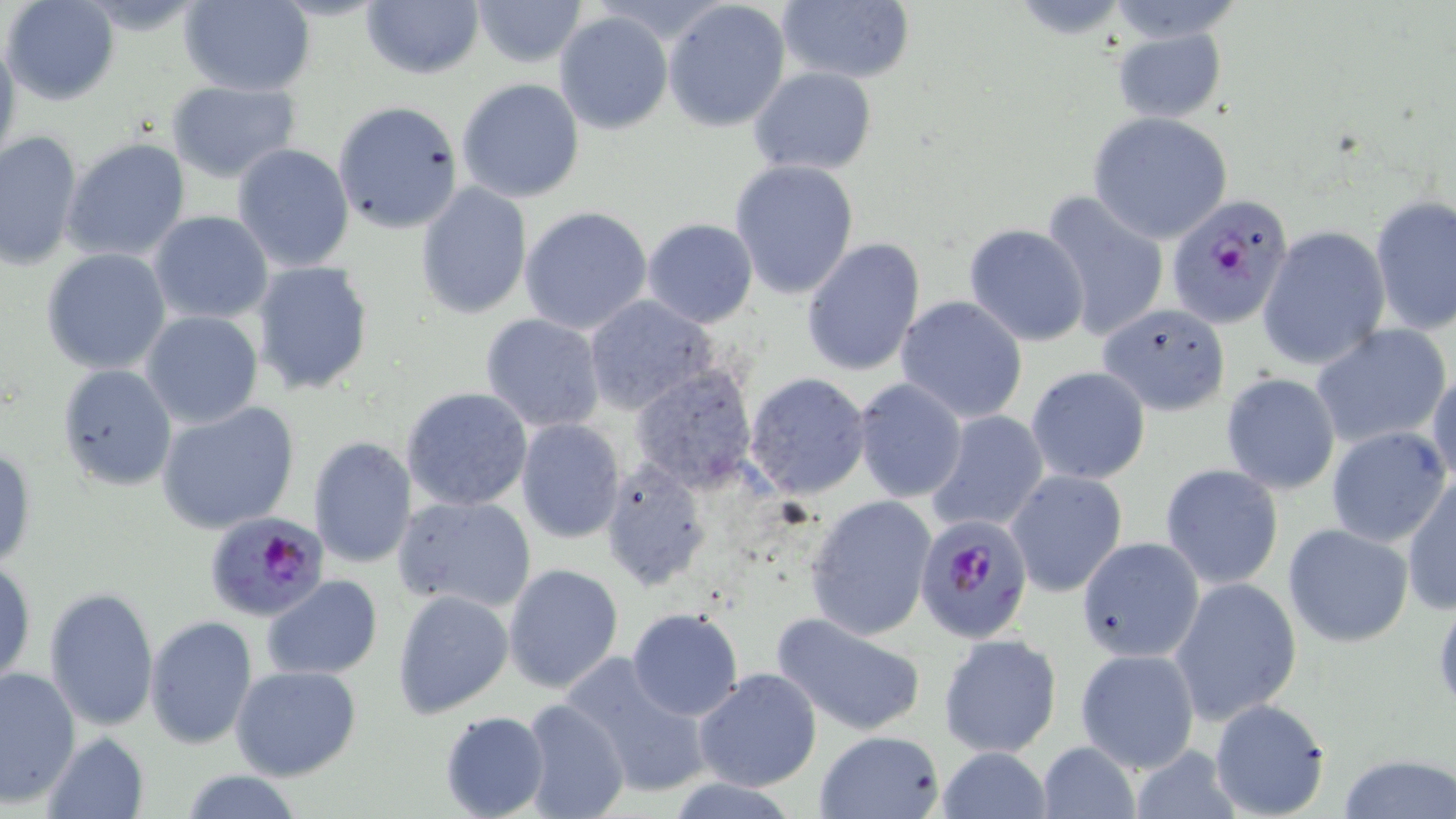
Approximate bounding boxes as named x1/y1/x2/y2 corners in pixels. Platelet locations: (x1=1431, y1=597, x2=1456, y2=714). Uninfected red blood cell locations: (x1=2, y1=0, x2=121, y2=106), (x1=177, y1=0, x2=314, y2=96), (x1=471, y1=0, x2=589, y2=69), (x1=662, y1=0, x2=792, y2=133), (x1=776, y1=0, x2=918, y2=86), (x1=360, y1=1, x2=485, y2=81), (x1=553, y1=9, x2=673, y2=134), (x1=1110, y1=28, x2=1227, y2=123), (x1=0, y1=31, x2=22, y2=172), (x1=476, y1=52, x2=645, y2=190), (x1=748, y1=67, x2=877, y2=176), (x1=457, y1=79, x2=585, y2=204), (x1=167, y1=81, x2=299, y2=181), (x1=332, y1=100, x2=464, y2=236), (x1=1087, y1=112, x2=1233, y2=245), (x1=0, y1=131, x2=83, y2=269), (x1=62, y1=137, x2=192, y2=263), (x1=232, y1=144, x2=355, y2=272), (x1=728, y1=160, x2=859, y2=300), (x1=415, y1=183, x2=530, y2=319), (x1=1039, y1=189, x2=1170, y2=343), (x1=1370, y1=195, x2=1455, y2=339), (x1=519, y1=205, x2=654, y2=336), (x1=150, y1=212, x2=273, y2=325), (x1=641, y1=216, x2=758, y2=327), (x1=963, y1=224, x2=1090, y2=346), (x1=1258, y1=225, x2=1390, y2=370), (x1=801, y1=239, x2=924, y2=377), (x1=41, y1=249, x2=171, y2=375), (x1=252, y1=262, x2=375, y2=396), (x1=583, y1=295, x2=718, y2=416), (x1=895, y1=296, x2=1028, y2=423), (x1=1097, y1=303, x2=1231, y2=416), (x1=141, y1=312, x2=264, y2=429), (x1=479, y1=312, x2=605, y2=433), (x1=1311, y1=324, x2=1451, y2=451), (x1=55, y1=364, x2=178, y2=491), (x1=629, y1=364, x2=758, y2=492), (x1=1026, y1=365, x2=1150, y2=486), (x1=1427, y1=368, x2=1456, y2=488), (x1=744, y1=372, x2=872, y2=498), (x1=1221, y1=372, x2=1340, y2=494), (x1=852, y1=377, x2=967, y2=503), (x1=400, y1=387, x2=533, y2=512), (x1=156, y1=402, x2=301, y2=534), (x1=927, y1=409, x2=1049, y2=534), (x1=515, y1=418, x2=625, y2=544), (x1=1326, y1=425, x2=1450, y2=546), (x1=307, y1=434, x2=418, y2=569), (x1=1, y1=444, x2=35, y2=567), (x1=598, y1=457, x2=712, y2=591), (x1=1159, y1=463, x2=1283, y2=592), (x1=1005, y1=469, x2=1129, y2=595), (x1=1403, y1=476, x2=1456, y2=615), (x1=805, y1=493, x2=937, y2=641), (x1=392, y1=494, x2=536, y2=613), (x1=1283, y1=522, x2=1414, y2=648), (x1=1077, y1=536, x2=1203, y2=662), (x1=1, y1=556, x2=36, y2=686), (x1=502, y1=564, x2=624, y2=692), (x1=261, y1=576, x2=382, y2=681), (x1=1169, y1=576, x2=1303, y2=724), (x1=43, y1=586, x2=159, y2=731), (x1=392, y1=588, x2=513, y2=718), (x1=627, y1=609, x2=744, y2=721), (x1=769, y1=610, x2=927, y2=737), (x1=144, y1=616, x2=258, y2=750), (x1=938, y1=633, x2=1062, y2=757), (x1=1075, y1=646, x2=1201, y2=774), (x1=563, y1=655, x2=714, y2=799), (x1=0, y1=665, x2=79, y2=805), (x1=231, y1=665, x2=362, y2=782), (x1=693, y1=668, x2=821, y2=791), (x1=520, y1=698, x2=630, y2=819), (x1=1208, y1=699, x2=1332, y2=819), (x1=440, y1=710, x2=550, y2=819), (x1=813, y1=729, x2=945, y2=819), (x1=43, y1=733, x2=149, y2=819), (x1=1035, y1=740, x2=1140, y2=818), (x1=1130, y1=744, x2=1241, y2=819), (x1=936, y1=748, x2=1054, y2=818), (x1=1337, y1=755, x2=1455, y2=819), (x1=176, y1=769, x2=305, y2=819), (x1=664, y1=778, x2=805, y2=818). Plasmodium falciparum-infected red blood cell locations: (x1=1167, y1=194, x2=1296, y2=331), (x1=202, y1=511, x2=332, y2=627), (x1=924, y1=517, x2=1027, y2=637). Slide-level diagnosis: Plasmodium falciparum. Image is 1456×819 pixels. Single field of view. Light microscopy. May-Grünwald-Giemsa-stained preparation. Thin blood smear. Captured at 1000x magnification.